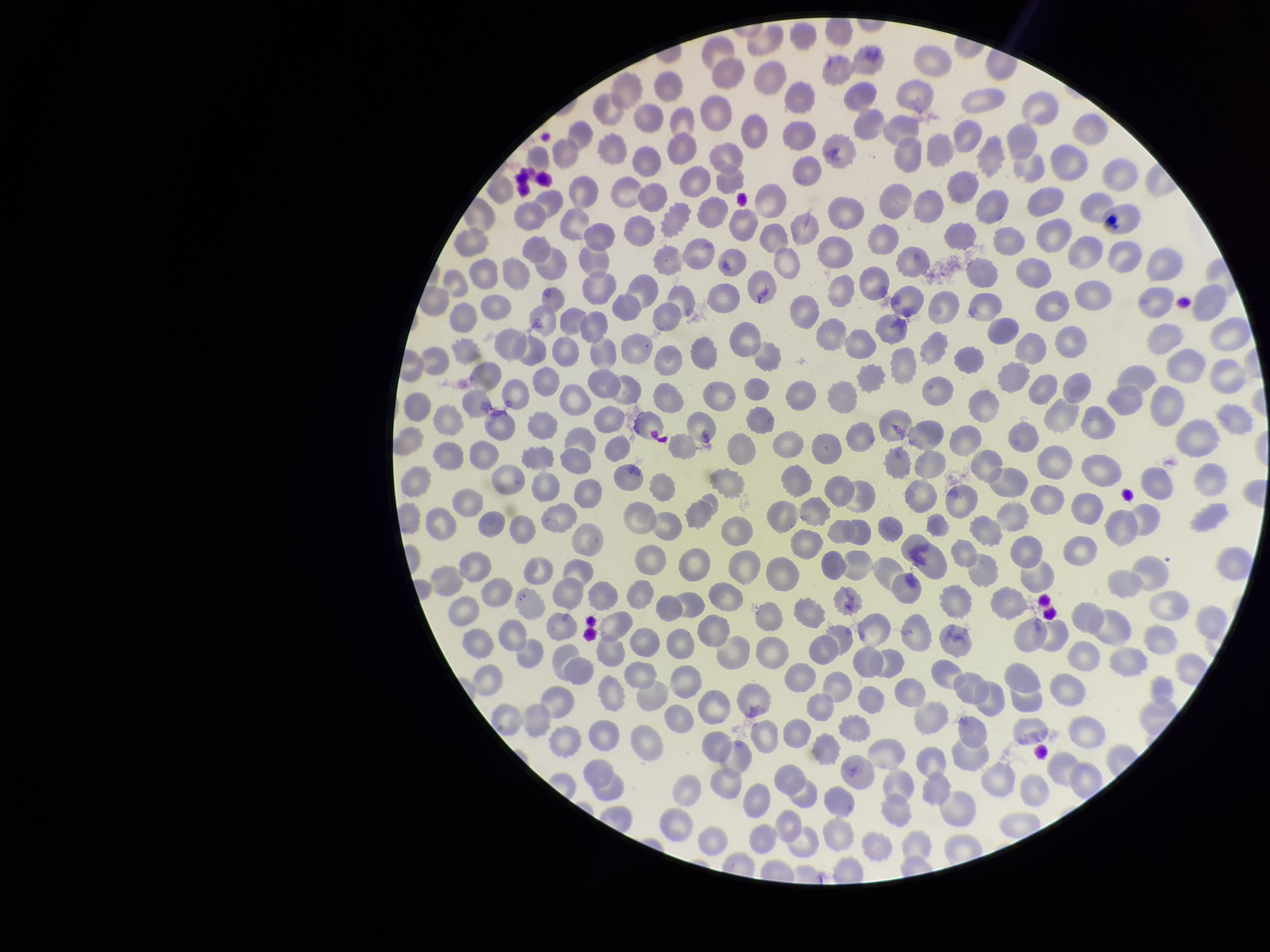
parasitized red blood cells = none identified
capture = smartphone photograph through the microscope eyepiece
stain = Giemsa
red blood cell count = 331
field of view = one from this slide
image size = 1270×952 pixels
preparation = thin
patient malaria status = infected
parasitized red blood cell count = 0
species reported for this patient = Plasmodium vivax